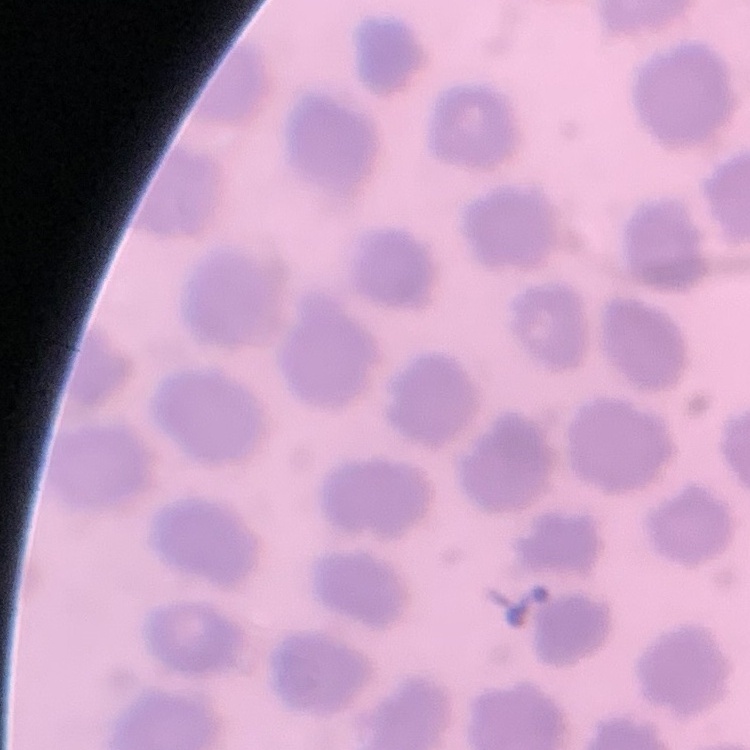

Summary:
  - Red blood cell morphology: no rouleaux formation
  - Stain: Field's or Giemsa
  - Image type: square crop of a larger photomicrograph
  - Preparation: thin peripheral smear